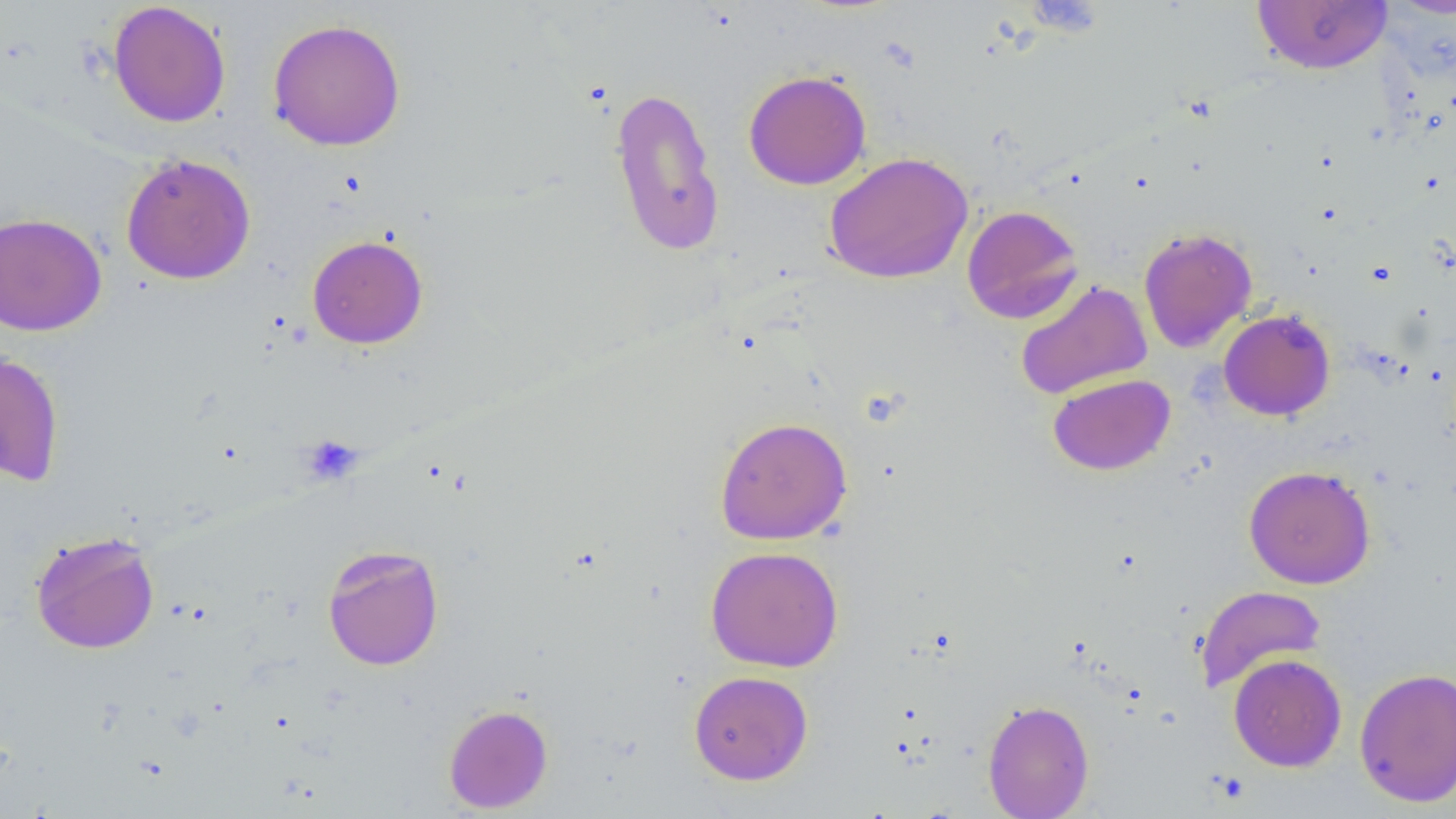
Approximate bounding boxes as (x1,y1)-(x2,y2) corner pairs in pixels. Platelet locations: (301,436)-(362,485). Uninfected red blood cell locations: (1251,0)-(1393,75), (107,2)-(232,128), (267,18)-(406,151), (743,69)-(872,190), (608,84)-(725,257), (824,151)-(973,284), (120,153)-(256,285), (962,205)-(1084,325), (0,212)-(107,336), (1139,227)-(1257,352), (307,235)-(428,349), (1015,280)-(1153,400), (1218,309)-(1336,420), (0,351)-(65,487), (1047,373)-(1175,476), (715,416)-(853,545), (1243,465)-(1376,589), (30,531)-(160,654), (322,545)-(444,671), (705,545)-(843,672), (1194,585)-(1327,694), (1228,653)-(1346,772), (1354,667)-(1456,806), (688,670)-(813,784), (982,699)-(1094,819), (444,704)-(553,813). Slide-level diagnosis: no evidence of blood parasites. Image is 1456×819 pixels. Single field of view. Thin blood smear. Light microscopy. 1000x magnification.